Report the malaria status of this cell.
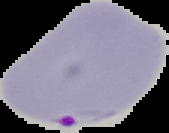

Parasitized.

image_size: 169×133 pixels
preparation: thin blood smear
image_type: cell region segmented out of the field of view; surrounding area masked to black